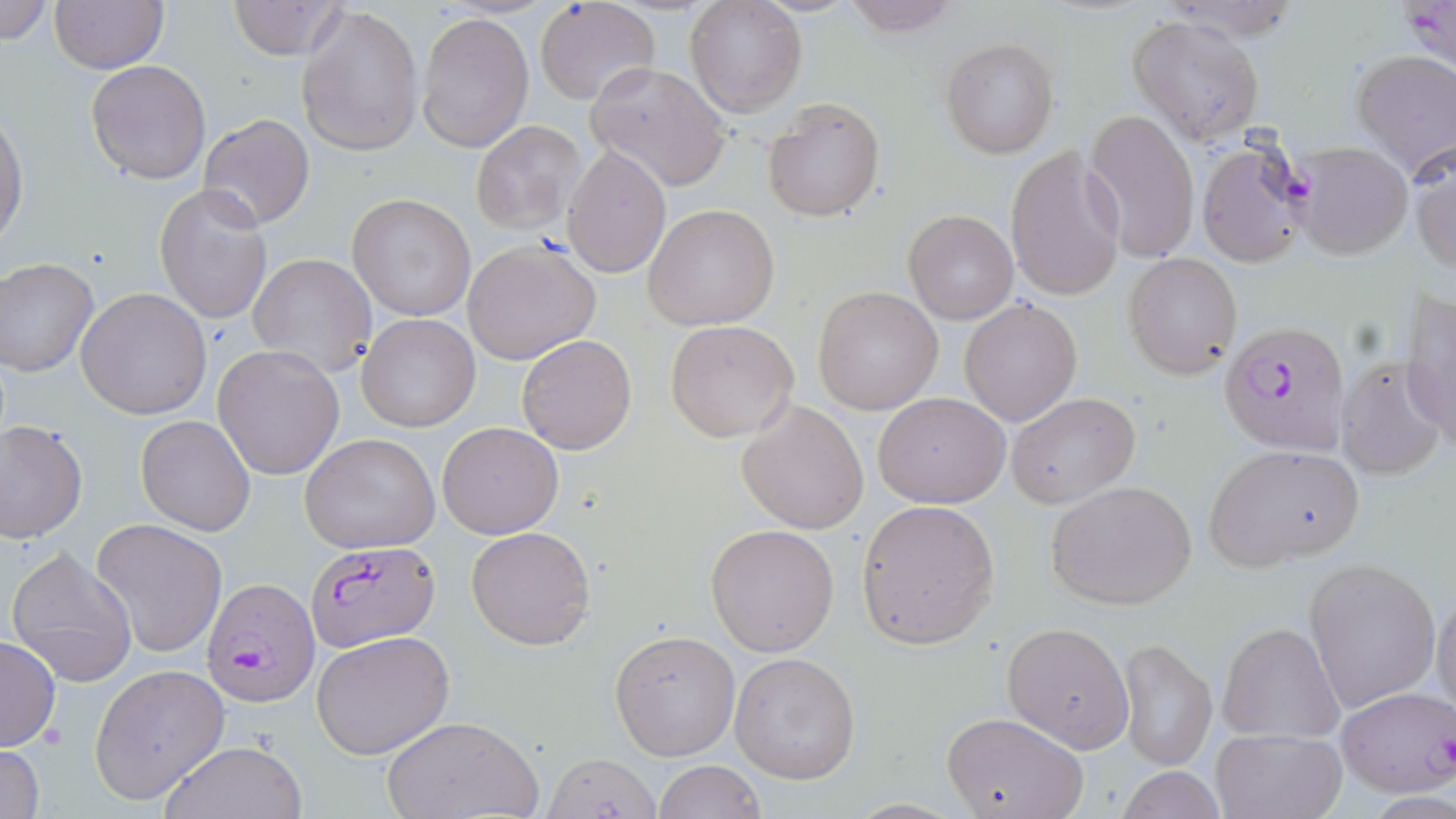
Summary:
  - Coordinate format: approximate bounding boxes as [x1, y1, x2, y2] in pixels
  - Uninfected red blood cell locations: [0, 0, 55, 48], [686, 0, 806, 119], [836, 0, 965, 38], [48, 1, 167, 73], [229, 1, 345, 60], [535, 2, 659, 107], [295, 4, 424, 158], [417, 12, 534, 153], [1127, 15, 1266, 146], [941, 37, 1060, 158], [1349, 50, 1456, 178], [86, 59, 212, 184], [585, 60, 732, 193], [764, 98, 885, 224], [0, 106, 29, 251], [1084, 110, 1200, 264], [199, 113, 315, 230], [471, 120, 586, 233], [1196, 134, 1314, 268], [1409, 140, 1455, 274], [562, 145, 671, 279], [1005, 145, 1127, 303], [154, 183, 273, 326], [346, 192, 475, 322], [644, 204, 779, 330], [903, 209, 1018, 324], [463, 239, 602, 365], [1124, 252, 1242, 379], [248, 253, 377, 377], [0, 257, 100, 377], [812, 285, 944, 414], [1402, 287, 1456, 443], [76, 288, 211, 419], [960, 298, 1082, 427], [357, 313, 481, 431], [665, 319, 801, 442], [516, 334, 637, 455], [213, 344, 346, 480], [1334, 356, 1448, 483], [874, 391, 1010, 507], [1006, 391, 1141, 508], [738, 400, 869, 533], [134, 414, 255, 537], [1, 420, 88, 543], [437, 422, 565, 538], [301, 434, 441, 553], [1205, 444, 1362, 567], [1046, 479, 1198, 612], [856, 500, 998, 648], [91, 519, 227, 658], [706, 522, 840, 656], [466, 525, 596, 650], [6, 546, 139, 687], [1302, 557, 1441, 714], [1431, 587, 1456, 724], [1218, 621, 1343, 744], [1002, 622, 1133, 751], [611, 628, 741, 760], [312, 630, 456, 759], [0, 634, 61, 751], [1117, 638, 1217, 771], [729, 651, 861, 782], [90, 664, 228, 803], [1337, 687, 1456, 798], [939, 711, 1089, 819], [384, 715, 540, 819], [1211, 728, 1348, 818], [156, 739, 309, 819], [0, 740, 46, 819], [549, 754, 661, 819], [652, 760, 765, 819], [1114, 767, 1229, 818]
  - Plasmodium falciparum-infected red blood cell locations: [1400, 0, 1455, 69], [1294, 141, 1411, 261], [1222, 320, 1350, 455], [307, 541, 439, 651], [204, 576, 321, 707]
  - Slide-level diagnosis: Plasmodium falciparum
  - Preparation: thin blood film
  - Image size: 1456×819 pixels
  - Stain: May-Grünwald-Giemsa
  - Magnification: 1000x
  - Modality: light microscopy
  - Field of view: one of a larger specimen